Name the cell type shown.
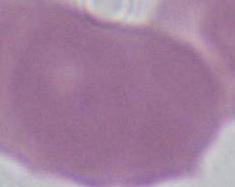

An erythrocyte.

Summary:
  - Magnification: 1000x
  - Modality: photomicrograph